Point out each Plasmodium parasite.
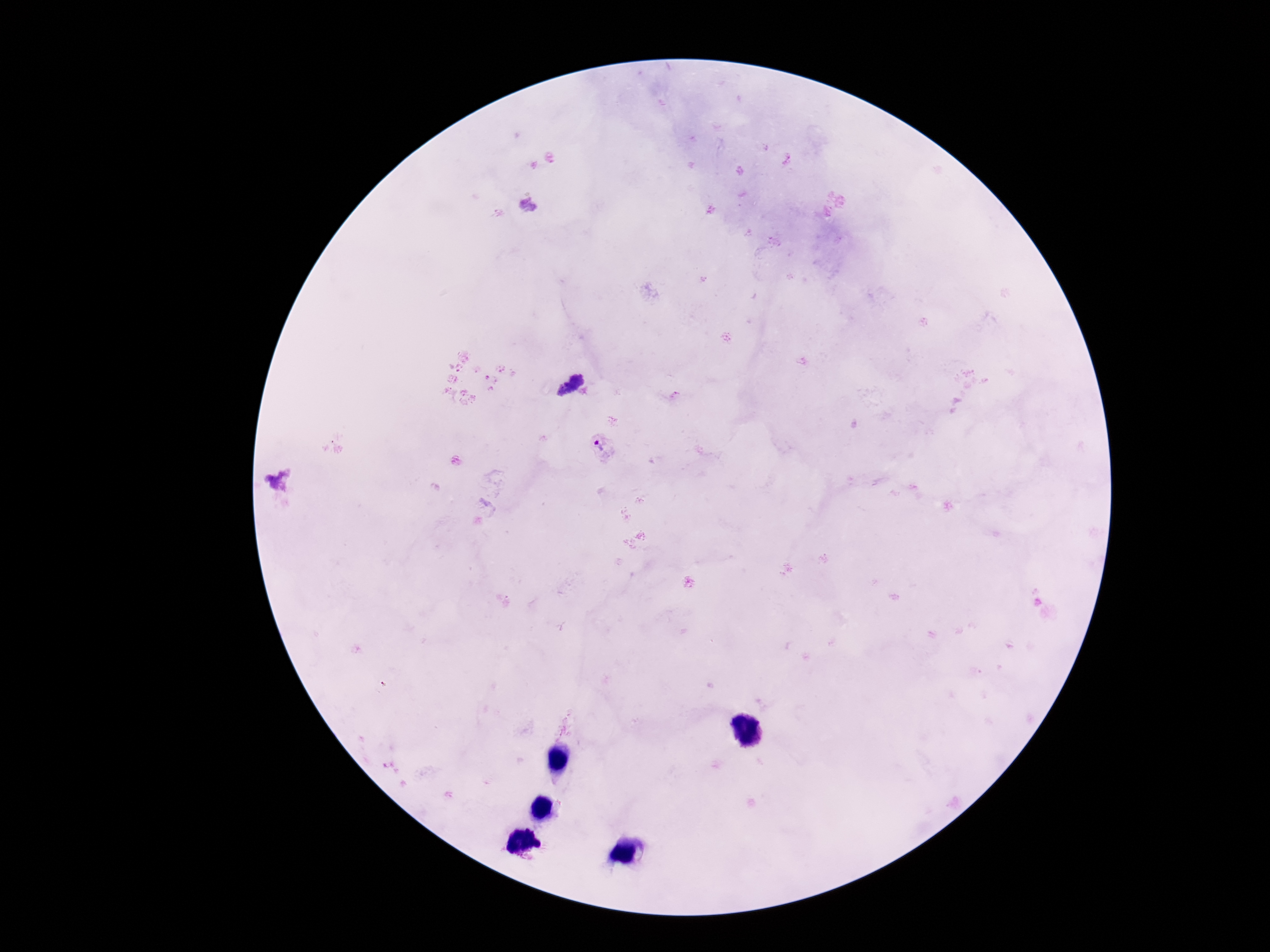

Approximate centers as [x, y] in pixels.
Plasmodium parasites: [571, 386], [600, 448].

{
  "field_of_view": "single",
  "image_size": "1270×952 pixels",
  "capture": "smartphone camera through the microscope eyepiece",
  "stain": "Giemsa",
  "patient_malaria_status": "infected",
  "magnification": "100x",
  "preparation": "thick blood film"
}